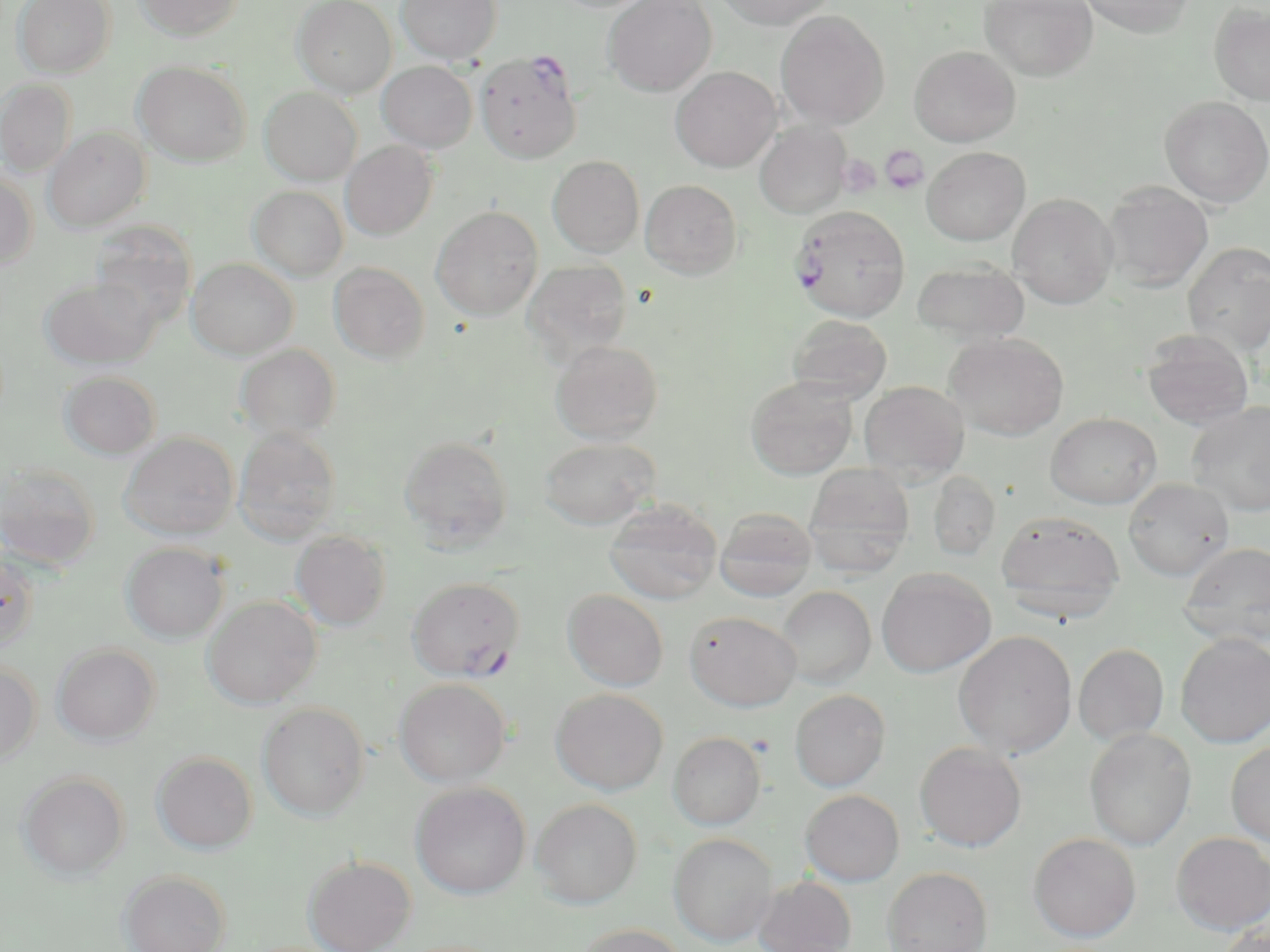

Approximate bounding boxes as named x1/y1/x2/y2 corners in pixels. Uninfected red blood cell locations: (x1=12, y1=0, x2=115, y2=78), (x1=136, y1=0, x2=244, y2=40), (x1=292, y1=0, x2=397, y2=97), (x1=396, y1=0, x2=502, y2=64), (x1=603, y1=0, x2=716, y2=96), (x1=714, y1=0, x2=835, y2=29), (x1=980, y1=0, x2=1098, y2=81), (x1=1077, y1=0, x2=1196, y2=37), (x1=1209, y1=2, x2=1269, y2=106), (x1=775, y1=10, x2=890, y2=129), (x1=909, y1=45, x2=1021, y2=146), (x1=133, y1=61, x2=251, y2=167), (x1=377, y1=61, x2=477, y2=153), (x1=671, y1=66, x2=781, y2=172), (x1=0, y1=78, x2=77, y2=177), (x1=260, y1=87, x2=362, y2=185), (x1=1159, y1=96, x2=1270, y2=208), (x1=754, y1=121, x2=851, y2=219), (x1=43, y1=127, x2=150, y2=232), (x1=341, y1=140, x2=438, y2=241), (x1=922, y1=146, x2=1030, y2=245), (x1=547, y1=155, x2=645, y2=257), (x1=0, y1=170, x2=37, y2=270), (x1=640, y1=180, x2=742, y2=279), (x1=1103, y1=180, x2=1213, y2=292), (x1=248, y1=185, x2=349, y2=281), (x1=1007, y1=193, x2=1118, y2=309), (x1=431, y1=205, x2=543, y2=320), (x1=91, y1=221, x2=198, y2=328), (x1=1182, y1=241, x2=1270, y2=355), (x1=187, y1=258, x2=298, y2=359), (x1=522, y1=259, x2=634, y2=363), (x1=913, y1=260, x2=1030, y2=346), (x1=329, y1=262, x2=430, y2=364), (x1=41, y1=277, x2=159, y2=370), (x1=786, y1=314, x2=892, y2=403), (x1=1141, y1=329, x2=1254, y2=429), (x1=945, y1=332, x2=1069, y2=441), (x1=550, y1=340, x2=663, y2=444), (x1=235, y1=343, x2=341, y2=442), (x1=59, y1=371, x2=162, y2=459), (x1=746, y1=376, x2=857, y2=479), (x1=859, y1=381, x2=969, y2=481), (x1=1187, y1=401, x2=1270, y2=516), (x1=1046, y1=412, x2=1161, y2=508), (x1=233, y1=427, x2=342, y2=544), (x1=120, y1=433, x2=238, y2=540), (x1=398, y1=436, x2=514, y2=548), (x1=538, y1=437, x2=659, y2=529), (x1=0, y1=462, x2=101, y2=571), (x1=803, y1=464, x2=915, y2=576), (x1=927, y1=470, x2=1001, y2=561), (x1=1123, y1=477, x2=1234, y2=580), (x1=604, y1=500, x2=722, y2=604), (x1=715, y1=508, x2=817, y2=601), (x1=996, y1=510, x2=1125, y2=620), (x1=291, y1=530, x2=392, y2=630), (x1=121, y1=542, x2=228, y2=643), (x1=1179, y1=543, x2=1270, y2=646), (x1=0, y1=552, x2=38, y2=651), (x1=876, y1=567, x2=996, y2=676), (x1=777, y1=585, x2=876, y2=688), (x1=563, y1=589, x2=669, y2=690), (x1=203, y1=595, x2=322, y2=709), (x1=684, y1=611, x2=801, y2=711), (x1=954, y1=631, x2=1076, y2=757), (x1=1176, y1=633, x2=1270, y2=748), (x1=52, y1=643, x2=160, y2=745), (x1=1073, y1=643, x2=1169, y2=745), (x1=0, y1=661, x2=42, y2=766), (x1=394, y1=678, x2=511, y2=787), (x1=551, y1=688, x2=668, y2=795), (x1=789, y1=689, x2=890, y2=791), (x1=257, y1=702, x2=370, y2=820), (x1=1084, y1=728, x2=1197, y2=850), (x1=668, y1=731, x2=766, y2=829), (x1=914, y1=742, x2=1027, y2=851), (x1=1225, y1=742, x2=1270, y2=846), (x1=152, y1=751, x2=257, y2=853), (x1=18, y1=771, x2=129, y2=880), (x1=410, y1=782, x2=531, y2=899), (x1=800, y1=789, x2=904, y2=886), (x1=530, y1=798, x2=642, y2=907), (x1=1028, y1=832, x2=1141, y2=942), (x1=1171, y1=832, x2=1270, y2=934), (x1=669, y1=833, x2=777, y2=946), (x1=303, y1=854, x2=416, y2=952), (x1=882, y1=866, x2=993, y2=952), (x1=118, y1=869, x2=231, y2=952), (x1=754, y1=876, x2=857, y2=952), (x1=1216, y1=920, x2=1270, y2=952), (x1=573, y1=923, x2=690, y2=952). Plasmodium falciparum-infected red blood cell locations: (x1=475, y1=52, x2=583, y2=164), (x1=789, y1=204, x2=911, y2=322), (x1=406, y1=577, x2=525, y2=681). Platelet locations: (x1=880, y1=146, x2=929, y2=196), (x1=838, y1=153, x2=879, y2=198). Slide-level diagnosis: Plasmodium falciparum. Single field of view. May-Grünwald-Giemsa stain. 1000x magnification. Image is 1270×952 pixels. Light microscopy. Thin blood smear.